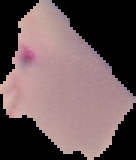
image size = 136×160 pixels
image type = segmented cell region with the area outside set to black
preparation = thin blood smear
malaria status = parasitized